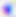
Toxoplasma gondii is shown. 400x magnification. Micrograph.